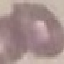 Malaria status: uninfected. Automatically extracted cell patch, resized to 64 × 64 pixels. Giemsa-stained preparation. Thin smear of blood. Acquired by smartphone through the microscope eyepiece.